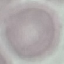
result = no malaria parasites seen
stain = Giemsa
preparation = thin blood smear
capture = smartphone camera at the microscope eyepiece
image type = cell patch, automatically extracted from a larger field of view and resized to 64 × 64 pixels